Give the position of every leukocyte.
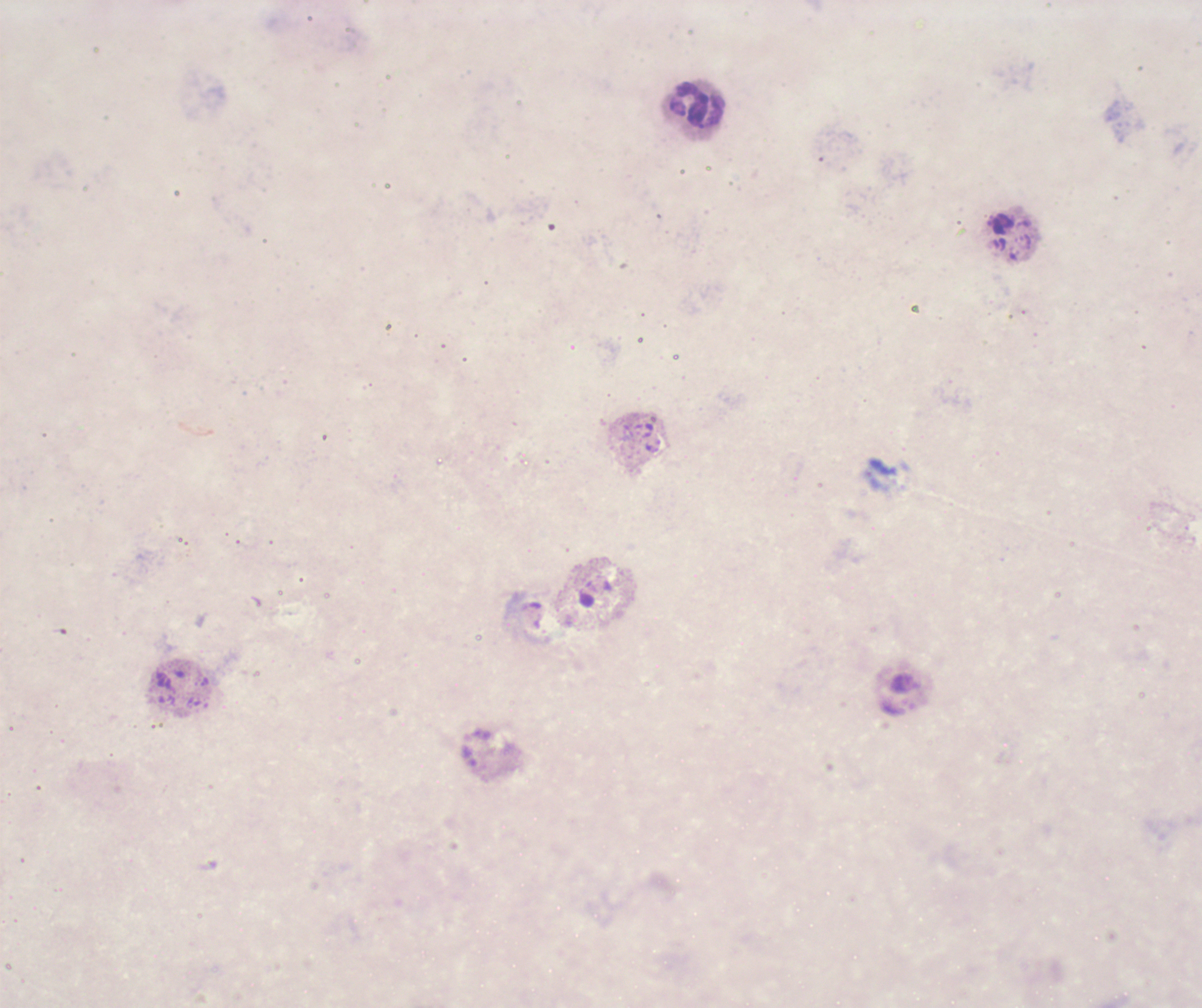

Approximate object centers, in pixels from the top-left corner.
Leukocytes: (x=698, y=103).

stain = Romanowsky
result = negative for malaria parasites
background quality = poor
image size = 1202×1008 pixels
coloration quality = bad
context = previously used in a real diagnosis
field of view = single
preparation = thick smear of blood
magnification = 100x